Identify the cell.
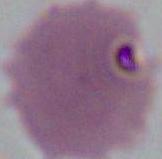

An erythrocyte.

1000x magnification. Micrograph.